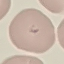 Malaria status: parasitized. Acquired by smartphone through the microscope eyepiece. Giemsa-stained preparation. Thin blood film. Cell patch, automatically extracted from a larger field of view and resized to 64 × 64 pixels.